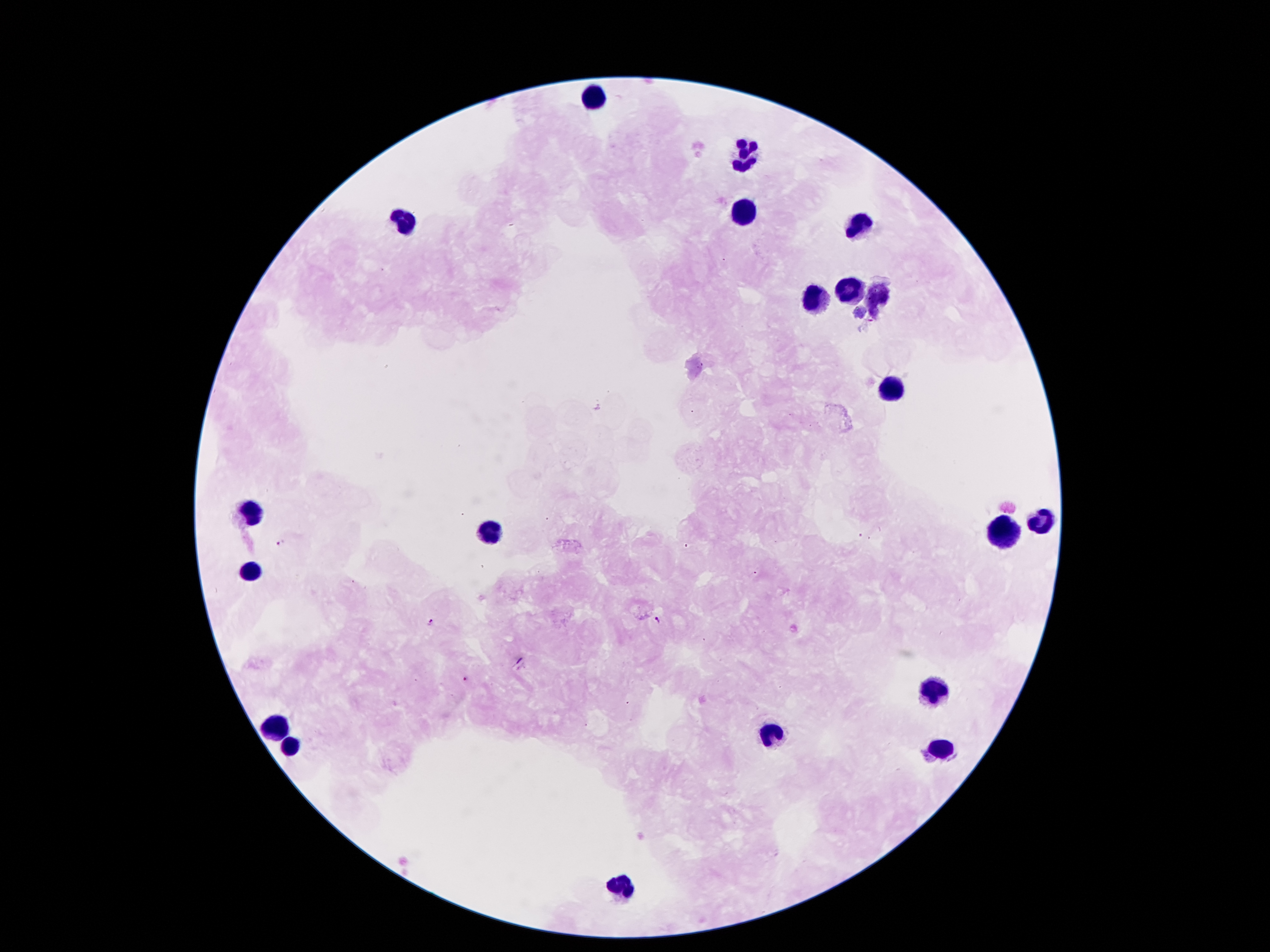

plasmodium_parasite_locations: 'approximate centers as (x, y) in pixels: (279, 542), (660, 620), (432, 622), (465, 678)'
capture: smartphone through the microscope eyepiece
stain: Giemsa
field_of_view: single
preparation: thick blood film
magnification: 100x
patient_malaria_status: positive for Plasmodium falciparum
leukocyte_locations: 'approximate centers as (x, y) in pixels: (593, 97), (744, 156), (740, 212), (404, 222), (858, 225), (848, 287), (875, 297), (815, 300), (893, 388), (253, 512), (1043, 517), (492, 531), (1005, 534), (247, 573), (934, 689), (279, 727), (772, 733), (290, 745), (944, 749), (622, 887)'
image_size: 1270×952 pixels